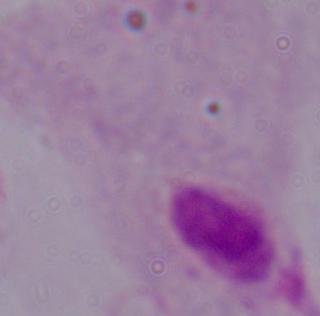
Summary:
  - Modality: micrograph
  - Magnification: 1000x
  - Identification: trichomonad